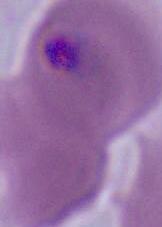
modality = micrograph
magnification = 400x or 1000x
identification = Plasmodium